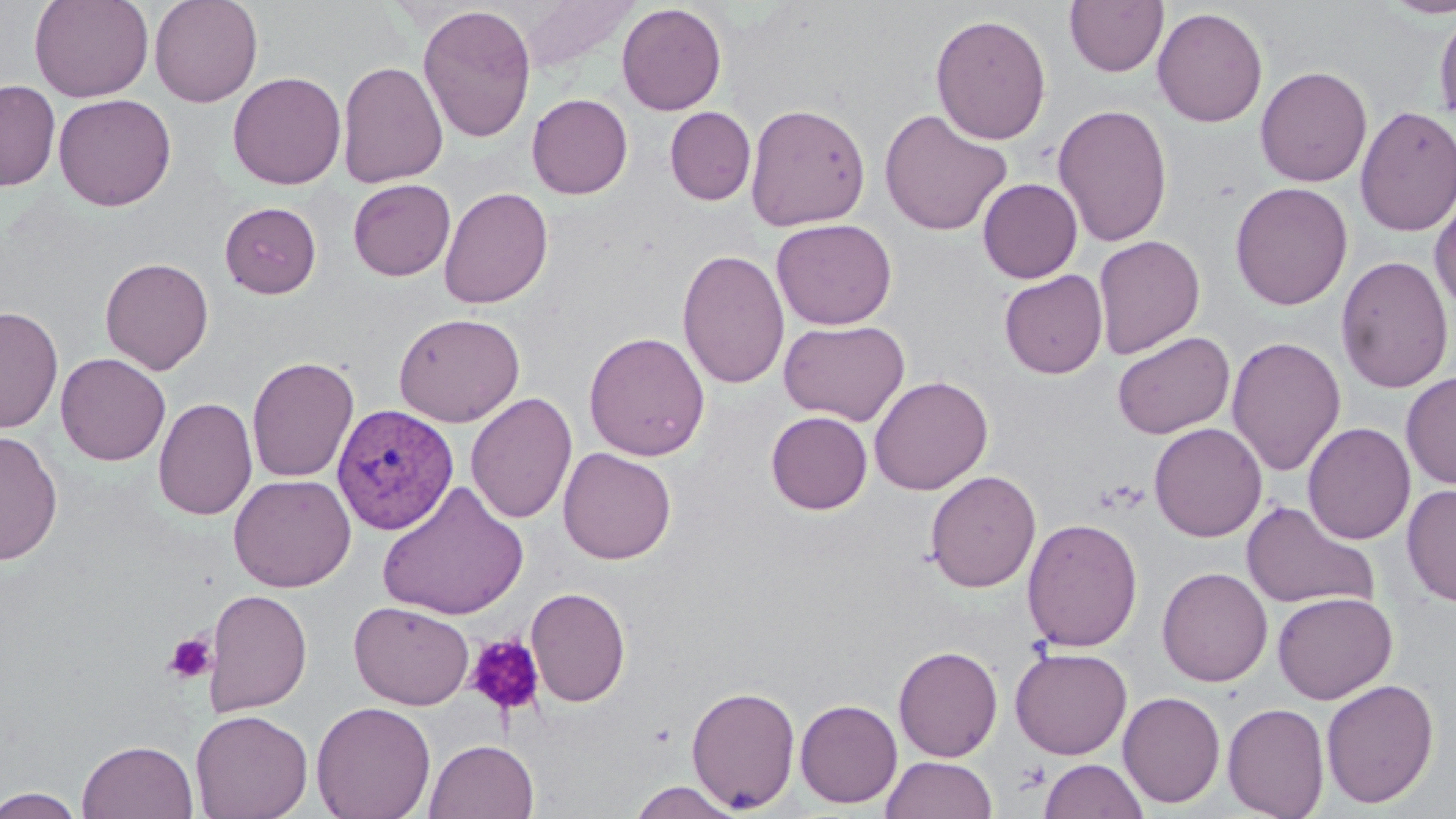

Plasmodium vivax-infected red blood cell locations = approximate bounding boxes as (x1, y1, x2, y2) in pixels: (331, 403, 458, 534)
slide-level diagnosis = Plasmodium vivax
magnification = 1000x
field of view = one of a larger specimen
platelet locations = approximate bounding boxes as (x1, y1, x2, y2) in pixels: (164, 632, 218, 684), (464, 634, 547, 718)
stain = May-Grünwald-Giemsa
uninfected red blood cell locations = approximate bounding boxes as (x1, y1, x2, y2) in pixels: (29, 0, 154, 102), (149, 0, 263, 107), (1064, 0, 1168, 78), (1379, 0, 1456, 20), (616, 3, 727, 116), (417, 4, 537, 143), (1152, 6, 1268, 127), (1434, 8, 1456, 127), (930, 13, 1052, 145), (337, 60, 448, 189), (1255, 65, 1373, 187), (227, 71, 346, 189), (0, 80, 61, 191), (53, 93, 176, 211), (527, 93, 633, 199), (744, 102, 872, 231), (1052, 103, 1174, 248), (1355, 105, 1456, 237), (664, 107, 756, 205), (879, 108, 1013, 237), (348, 178, 456, 281), (977, 178, 1082, 283), (1229, 182, 1353, 310), (438, 187, 553, 309), (1429, 193, 1456, 316), (220, 202, 321, 298), (771, 218, 897, 330), (1093, 234, 1206, 359), (677, 249, 790, 390), (1335, 255, 1454, 394), (99, 257, 214, 374), (999, 270, 1108, 379), (0, 305, 64, 434), (393, 311, 525, 427), (779, 319, 910, 426), (584, 331, 710, 461), (1111, 331, 1235, 439), (1226, 336, 1346, 476), (56, 352, 170, 465), (246, 355, 359, 483), (1401, 371, 1456, 489), (869, 374, 993, 495), (465, 392, 578, 525), (152, 396, 257, 521), (765, 410, 872, 514), (1149, 422, 1267, 542), (1303, 422, 1415, 545), (0, 430, 63, 566), (558, 447, 676, 564), (924, 469, 1041, 593), (228, 473, 356, 592), (378, 481, 529, 620), (1401, 483, 1456, 607), (1240, 500, 1379, 612), (1022, 517, 1143, 653), (1157, 566, 1273, 687), (203, 587, 312, 717), (525, 587, 631, 707), (1272, 591, 1397, 704), (349, 600, 474, 710), (893, 645, 1003, 762), (1010, 647, 1132, 759), (1321, 677, 1439, 808), (686, 684, 801, 813), (1118, 690, 1225, 808), (795, 699, 903, 808), (311, 701, 436, 819), (1222, 702, 1330, 819), (190, 709, 313, 819), (76, 739, 199, 819), (424, 739, 539, 819), (882, 756, 996, 818), (1038, 758, 1149, 819), (627, 781, 746, 818), (1, 787, 85, 818)
preparation = thin blood smear
modality = optical microscopy
image size = 1456×819 pixels